Identify the parasite.
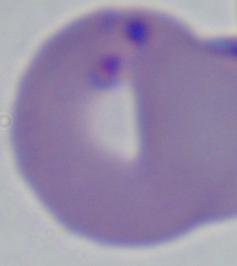
This is Babesia.

Summary:
  - Modality: micrograph
  - Magnification: 1000x